Name the parasite shown.
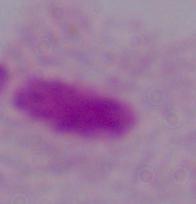
A trichomonad.

1000x magnification. Micrograph.